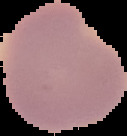
Segmented cell region on a black background. Image is 127×136 pixels. From a thin blood film. Result: negative for malaria parasites.